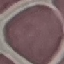

Summary:
  - Result: no malaria parasites detected
  - Stain: Giemsa
  - Image type: automatically extracted cell patch, resized to 64 × 64 pixels
  - Preparation: thin blood smear
  - Capture: smartphone camera at the microscope eyepiece